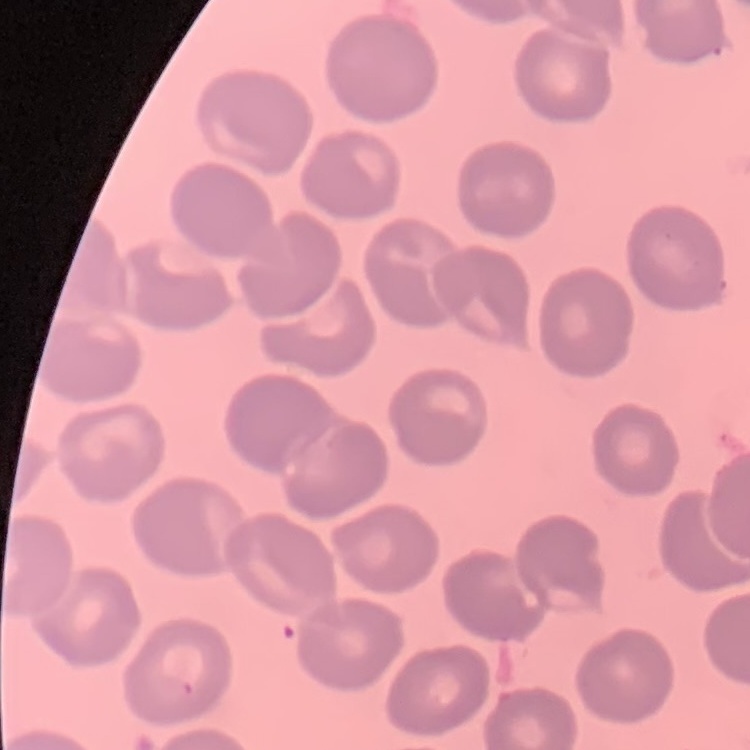
erythrocyte morphology = no rouleaux formation
image type = one tile cut from a larger photomicrograph
preparation = thin blood smear
stain = Field's or Giemsa